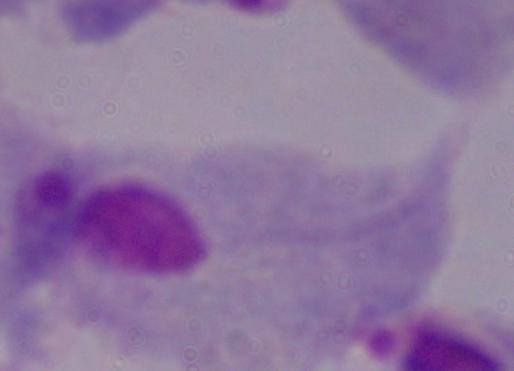

Photomicrograph. Captured at 1000x magnification. A trichomonad is shown.